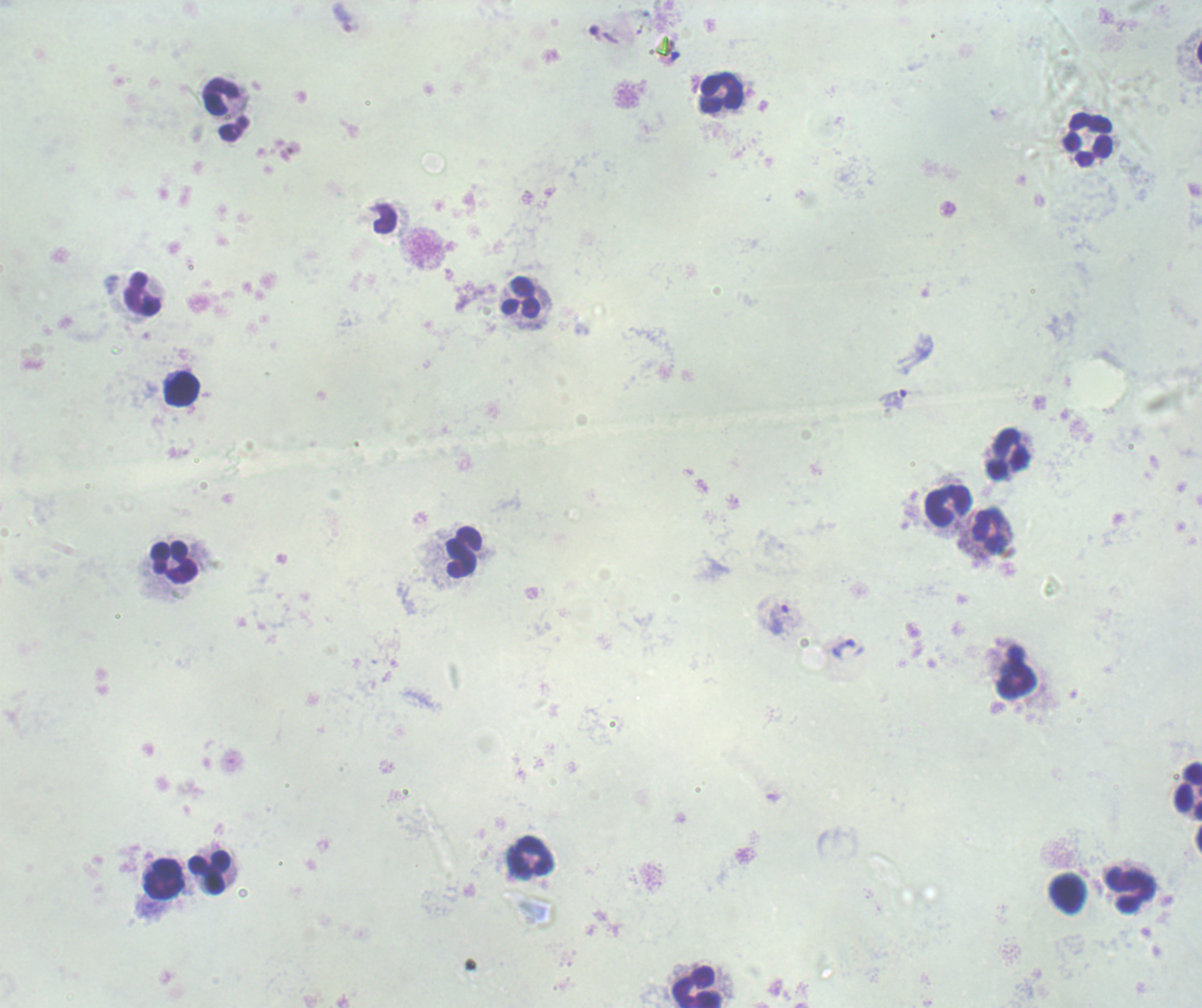

background_quality: poor
context: previously used in an actual diagnosis
image_size: 1202×1008 pixels
preparation: thick blood smear
result: malaria parasites identified
magnification: 100x
field_of_view: single
stain: Romanowsky
trophozoite_locations: 'approximate centers as (x, y) in pixels: (895, 400), (778, 619), (843, 650)'
leukocyte_locations: 'approximate centers as (x, y) in pixels: (721, 93), (221, 97), (1088, 139), (143, 294), (521, 297), (181, 390), (1008, 453), (948, 506), (990, 530), (464, 552), (174, 563), (1016, 679), (1186, 790), (531, 857), (209, 872), (164, 879), (1128, 890), (1069, 893), (698, 988)'